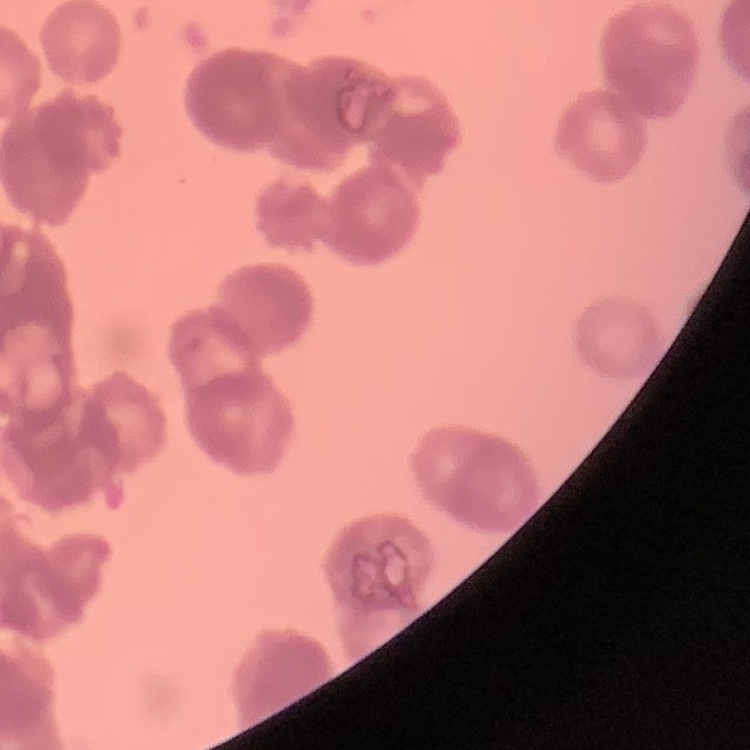

Summary:
  - Erythrocyte morphology: rouleaux formation
  - Stain: Field's or Giemsa
  - Preparation: thin peripheral smear
  - Image type: square crop of a larger photomicrograph